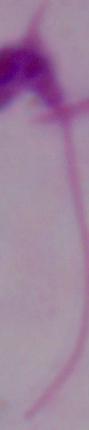

Captured at 1000x magnification. A Leishmania parasite is shown. Photomicrograph.